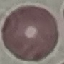
Result: no malaria parasites detected. Giemsa stain. Photographed with a smartphone camera at the microscope eyepiece. Thin blood smear. Automatically extracted cell patch, resized to 64 × 64 pixels.